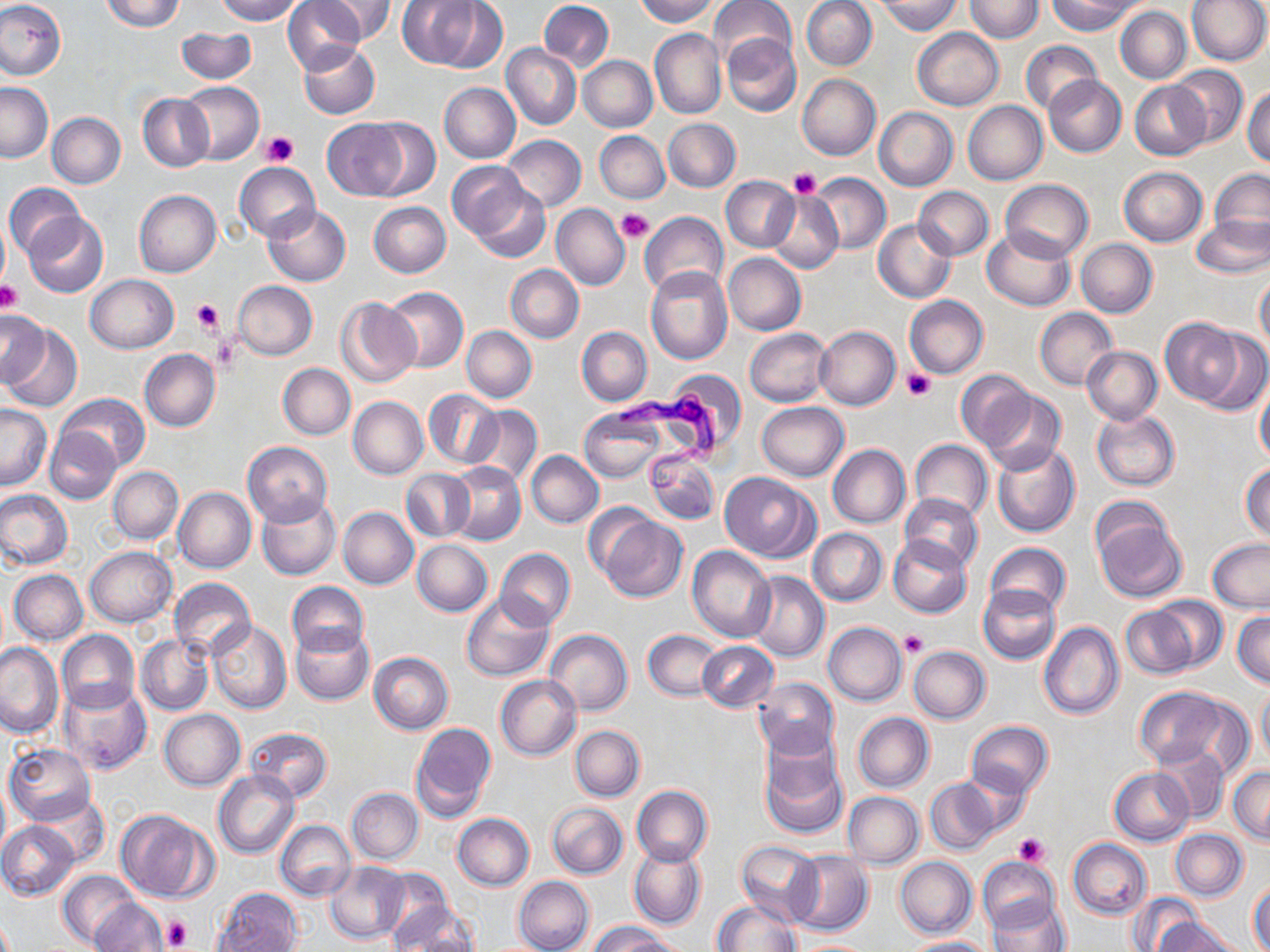
slide-level diagnosis = Trypanosoma brucei
preparation = thin blood smear
stain = May-Grünwald-Giemsa
Trypanosoma brucei locations = approximate bounding boxes as (x1, y1, x2, y2) in pixels: (612, 388, 723, 497)
magnification = 1000x
field of view = single
uninfected red blood cell locations = approximate bounding boxes as (x1, y1, x2, y2) in pixels: (0, 0, 67, 81), (102, 0, 184, 31), (215, 0, 302, 23), (283, 0, 364, 73), (317, 0, 398, 42), (396, 0, 482, 68), (537, 0, 614, 72), (634, 0, 718, 25), (709, 0, 796, 72), (800, 0, 877, 71), (878, 0, 960, 35), (964, 0, 1044, 42), (1049, 0, 1139, 35), (1186, 1, 1269, 67), (430, 2, 507, 72), (1115, 6, 1191, 83), (510, 14, 609, 114), (176, 27, 257, 85), (912, 28, 1004, 110), (650, 29, 727, 120), (720, 34, 801, 118), (1021, 40, 1101, 115), (299, 42, 379, 120), (501, 44, 581, 130), (578, 56, 656, 132), (1168, 65, 1248, 147), (796, 74, 880, 160), (1043, 75, 1126, 157), (1130, 80, 1211, 160), (179, 81, 264, 165), (0, 82, 53, 162), (439, 83, 521, 162), (1243, 85, 1270, 165), (138, 94, 214, 171), (963, 100, 1047, 184), (874, 108, 958, 191), (47, 112, 126, 189), (323, 118, 410, 198), (363, 118, 442, 201), (662, 119, 740, 192), (594, 131, 669, 203), (502, 135, 586, 212), (448, 161, 530, 243), (234, 162, 320, 243), (1119, 166, 1207, 245), (1209, 169, 1269, 245), (805, 172, 890, 255), (721, 176, 799, 252), (1000, 179, 1093, 263), (466, 182, 550, 262), (5, 183, 84, 260), (914, 186, 993, 260), (134, 190, 222, 277), (766, 191, 845, 274), (369, 202, 450, 278), (551, 204, 629, 290), (263, 205, 350, 285), (639, 210, 728, 297), (24, 213, 108, 298), (0, 215, 10, 292), (1192, 216, 1270, 278), (873, 219, 956, 302), (982, 228, 1075, 311), (1075, 239, 1158, 318), (724, 252, 806, 335), (506, 265, 584, 342), (644, 266, 732, 365), (1255, 273, 1269, 353), (85, 274, 176, 353), (232, 280, 318, 360), (384, 287, 467, 373), (905, 295, 988, 379), (336, 298, 421, 388), (1035, 307, 1118, 390), (0, 310, 47, 388), (1160, 317, 1244, 405), (1, 325, 82, 412), (462, 326, 537, 403), (576, 326, 653, 406), (815, 326, 900, 410), (745, 328, 833, 407), (1198, 332, 1270, 415), (1081, 346, 1162, 424), (139, 349, 220, 431), (277, 364, 354, 439), (663, 370, 747, 454), (956, 370, 1033, 452), (1255, 380, 1270, 465), (979, 388, 1066, 475), (424, 389, 502, 470), (56, 393, 149, 471), (348, 396, 428, 479), (756, 401, 849, 480), (1, 405, 51, 491), (467, 405, 542, 486), (579, 407, 665, 481), (1091, 409, 1180, 491), (45, 426, 122, 504), (910, 439, 992, 521), (243, 441, 333, 526), (991, 441, 1080, 538), (827, 444, 910, 528), (644, 448, 720, 526), (526, 451, 604, 528), (446, 462, 526, 546), (1241, 463, 1270, 542), (108, 467, 183, 543), (402, 469, 474, 541), (719, 471, 819, 562), (174, 487, 256, 573), (0, 490, 73, 570), (900, 493, 983, 571), (257, 495, 340, 580), (1090, 503, 1188, 604), (337, 507, 418, 589), (597, 513, 688, 603), (808, 527, 887, 606), (887, 535, 972, 617), (1207, 538, 1270, 612), (411, 539, 492, 616), (986, 543, 1070, 618), (85, 546, 176, 627), (688, 547, 776, 641), (495, 548, 575, 631), (9, 569, 87, 645), (746, 570, 830, 662), (167, 577, 255, 660), (287, 581, 369, 658), (979, 584, 1061, 663), (462, 595, 554, 681), (1149, 596, 1228, 671), (989, 597, 1101, 688), (1119, 602, 1202, 678), (1233, 611, 1269, 688), (207, 619, 293, 714), (1038, 620, 1123, 719), (823, 621, 907, 706), (291, 625, 373, 705), (56, 629, 140, 714), (545, 629, 633, 716), (644, 629, 722, 700), (137, 633, 215, 715), (696, 641, 778, 712), (0, 642, 65, 737), (909, 646, 990, 724), (367, 652, 453, 734), (495, 676, 581, 760), (751, 677, 839, 758), (58, 682, 152, 776), (1133, 686, 1239, 771), (1257, 687, 1270, 767), (159, 709, 244, 790), (853, 712, 933, 793), (409, 720, 495, 822), (966, 721, 1053, 797), (244, 726, 332, 802), (570, 726, 645, 801), (758, 734, 848, 839), (1151, 742, 1227, 823), (4, 743, 97, 825), (1228, 765, 1270, 844), (1108, 766, 1194, 845), (959, 768, 1031, 837), (213, 771, 299, 858), (925, 779, 999, 855), (0, 780, 10, 859), (631, 785, 712, 866), (346, 788, 423, 864), (843, 791, 924, 868), (31, 794, 109, 867), (547, 801, 628, 879), (116, 808, 216, 902), (453, 813, 535, 890), (275, 819, 356, 902), (0, 821, 79, 900), (1171, 829, 1247, 900), (1068, 839, 1151, 920), (736, 840, 825, 928), (630, 845, 704, 928), (785, 851, 873, 937), (894, 855, 976, 938), (978, 857, 1061, 934), (324, 861, 409, 945), (58, 869, 140, 950), (513, 876, 593, 952), (1249, 881, 1270, 950), (381, 882, 462, 952), (212, 886, 300, 951), (1129, 893, 1202, 952), (92, 899, 168, 952), (712, 899, 800, 952), (986, 900, 1069, 952), (1153, 915, 1241, 952), (589, 920, 677, 952), (900, 936, 992, 952)
platelet locations = approximate bounding boxes as (x1, y1, x2, y2) in pixels: (262, 130, 299, 166), (789, 167, 822, 198), (617, 209, 654, 243), (1, 283, 23, 313), (191, 296, 223, 333), (213, 332, 241, 372), (902, 368, 935, 401), (901, 630, 928, 657), (1013, 833, 1050, 866), (161, 914, 193, 951)
image size = 1270×952 pixels
modality = optical microscopy